Report the malaria status of this cell.
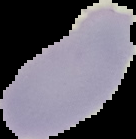

Uninfected.

From a thin blood film. Image is 136×139 pixels. Cell region segmented out of the field of view; the surrounding area is masked to black.